Find each parasitized red blood cell.
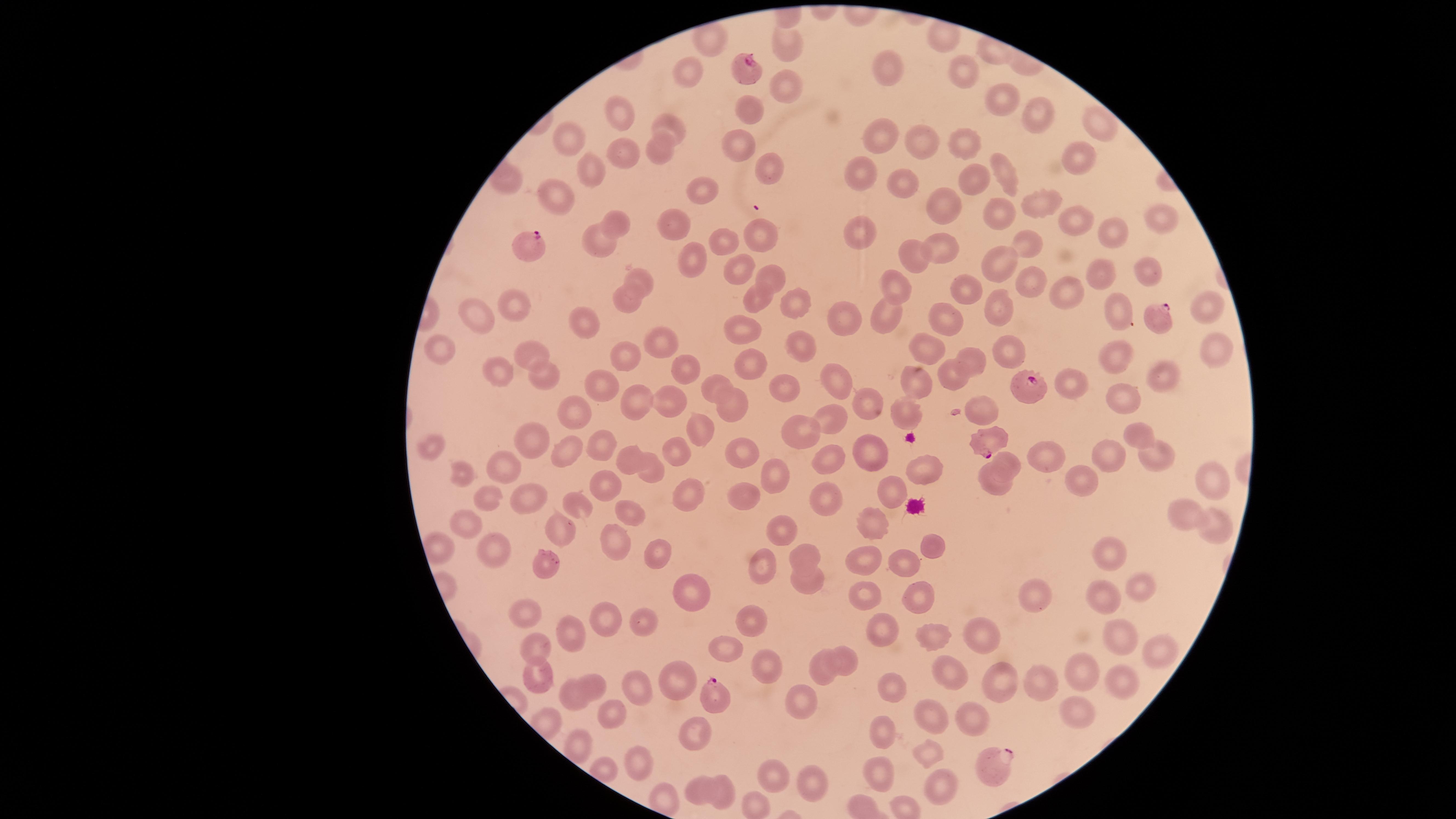
Approximate marker points as [x, y] in pixels.
Parasitized red blood cells: [753, 68], [526, 248], [1158, 313], [1029, 393], [980, 440], [710, 694], [993, 765].

Approximate marker points as [x, y] in pixels. Uninfected red blood cells: [707, 39], [939, 39], [788, 41], [962, 69], [886, 73], [689, 74], [787, 80], [994, 98], [615, 106], [751, 114], [1030, 117], [668, 122], [1097, 132], [569, 139], [915, 139], [876, 143], [960, 144], [661, 147], [737, 150], [622, 154], [1075, 158], [768, 169], [587, 172], [1002, 172], [856, 173], [968, 175], [506, 179], [899, 181], [701, 191], [558, 198], [938, 201], [1043, 210], [998, 214], [1072, 222], [619, 223], [1158, 223], [676, 225], [755, 233], [1103, 234], [860, 239], [943, 242], [1030, 242], [725, 243], [602, 247], [913, 256], [697, 258], [995, 267], [733, 271], [1148, 272], [638, 276], [775, 277], [1102, 279], [1029, 280], [898, 284], [966, 291], [1059, 295], [628, 297], [757, 299], [516, 302], [795, 302], [1203, 308], [481, 313], [1110, 313], [838, 314], [998, 314], [892, 315], [950, 320], [587, 324], [745, 329], [662, 342], [442, 345], [804, 349], [538, 350], [929, 353], [1204, 353], [626, 355], [1119, 355], [1002, 357], [976, 361], [752, 367], [685, 371], [505, 373], [546, 375], [915, 377], [948, 378], [1157, 378], [838, 379], [714, 386], [783, 386], [595, 387], [1073, 391], [667, 400], [730, 401], [1123, 402], [637, 405], [869, 408], [982, 409], [899, 411], [572, 415], [832, 422], [702, 425], [802, 435], [1140, 436], [529, 443], [603, 445], [432, 446], [873, 446], [564, 449], [743, 450], [674, 451], [633, 456], [1045, 458], [1160, 458], [1108, 459], [502, 462], [1005, 462], [833, 463], [923, 466], [772, 474], [650, 475], [462, 476], [1213, 478], [1075, 481], [605, 483], [996, 483], [897, 491], [823, 493], [690, 494], [525, 495], [749, 500], [490, 504], [578, 506], [630, 507], [1181, 519], [465, 521], [1215, 523], [875, 528], [563, 531], [781, 531], [932, 544], [619, 546], [492, 547], [1112, 547], [804, 553], [652, 555], [866, 565], [904, 565], [762, 567], [547, 571], [806, 579], [1138, 588], [1032, 594], [696, 595], [867, 595], [919, 599], [1099, 601], [518, 616], [608, 616], [749, 616], [646, 619], [881, 628], [564, 633], [979, 634], [1114, 635], [931, 638], [540, 647], [733, 650], [1165, 650], [848, 660], [768, 663], [948, 670], [537, 671], [1080, 671], [821, 672], [1118, 681], [669, 682], [1043, 682], [640, 683], [1005, 684], [598, 685], [889, 690], [567, 696], [805, 702], [608, 710], [1072, 711], [972, 718], [930, 720], [686, 726], [882, 733], [930, 754], [637, 766], [879, 771], [779, 776], [807, 783], [726, 785], [939, 788], [697, 789]. Giemsa stain. Photographed with a smartphone camera through the microscope eyepiece. The visible region is circular. Image is 1456×819 pixels. Thin blood smear. Single field of view. Species: Plasmodium falciparum.